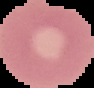
image_type: segmented cell region with the area outside set to black
preparation: thin blood film
malaria_status: uninfected
image_size: 94×88 pixels